Identify the blood parasite species.
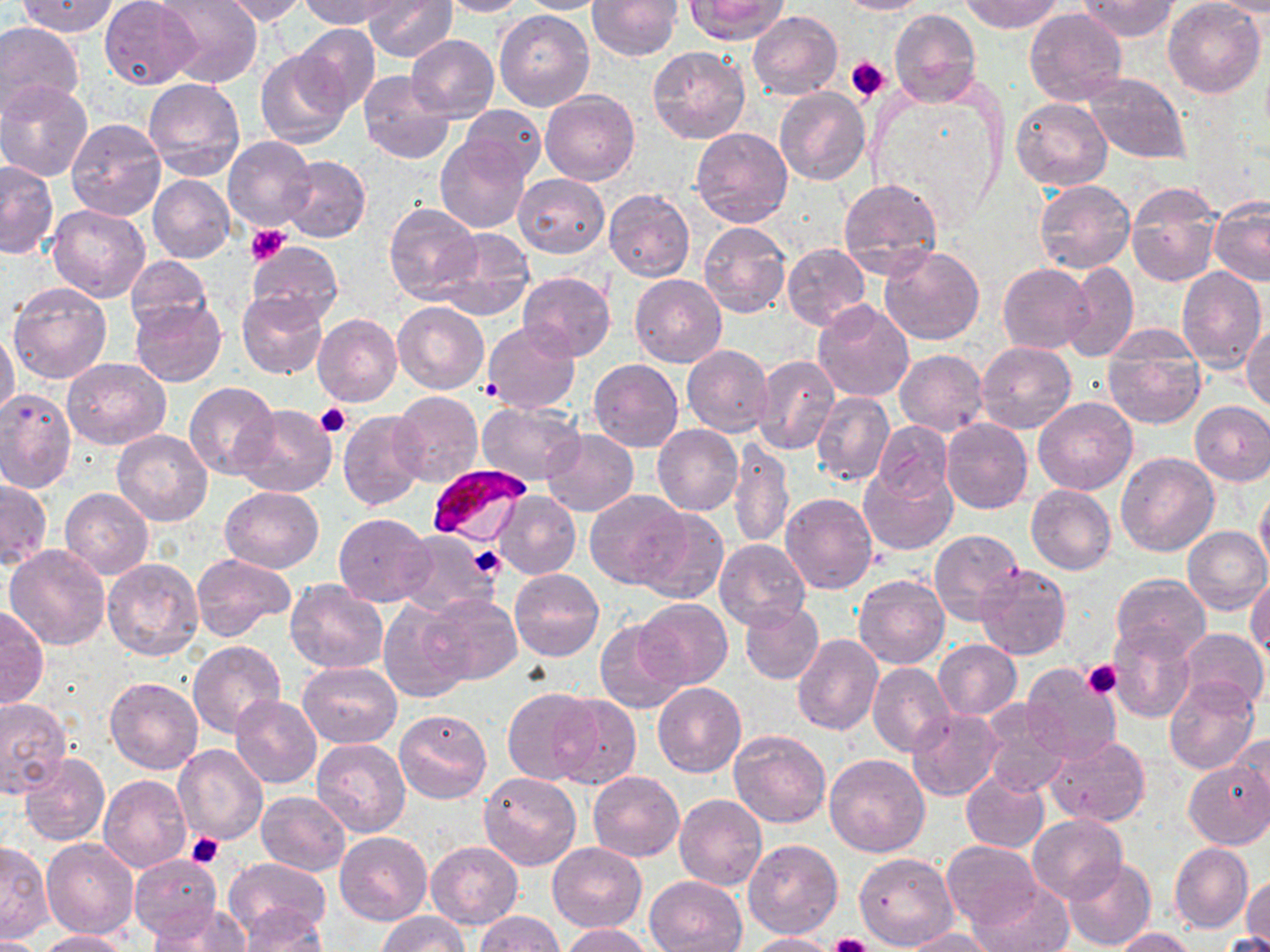

Plasmodium falciparum.

Approximate bounding boxes as named x1/y1/x2/y2 corners in pixels. Platelet locations: (x1=846, y1=55, x2=892, y2=101), (x1=244, y1=225, x2=291, y2=266), (x1=480, y1=379, x2=503, y2=403), (x1=316, y1=403, x2=352, y2=438), (x1=468, y1=546, x2=505, y2=577), (x1=1082, y1=659, x2=1121, y2=700), (x1=186, y1=833, x2=223, y2=869), (x1=826, y1=933, x2=875, y2=952). Uninfected red blood cell locations: (x1=17, y1=0, x2=119, y2=36), (x1=99, y1=0, x2=201, y2=88), (x1=154, y1=0, x2=262, y2=88), (x1=210, y1=0, x2=313, y2=25), (x1=301, y1=0, x2=396, y2=28), (x1=361, y1=0, x2=457, y2=62), (x1=436, y1=0, x2=527, y2=16), (x1=515, y1=0, x2=613, y2=13), (x1=586, y1=0, x2=681, y2=60), (x1=685, y1=0, x2=787, y2=44), (x1=835, y1=0, x2=931, y2=14), (x1=961, y1=0, x2=1062, y2=33), (x1=1076, y1=0, x2=1181, y2=40), (x1=1164, y1=1, x2=1265, y2=99), (x1=1207, y1=1, x2=1270, y2=15), (x1=495, y1=8, x2=594, y2=111), (x1=1024, y1=8, x2=1127, y2=108), (x1=890, y1=9, x2=982, y2=109), (x1=748, y1=10, x2=843, y2=100), (x1=0, y1=23, x2=83, y2=119), (x1=294, y1=25, x2=381, y2=112), (x1=407, y1=35, x2=498, y2=121), (x1=647, y1=45, x2=751, y2=144), (x1=255, y1=48, x2=351, y2=149), (x1=357, y1=70, x2=455, y2=164), (x1=1085, y1=73, x2=1190, y2=165), (x1=144, y1=79, x2=245, y2=182), (x1=0, y1=82, x2=92, y2=182), (x1=774, y1=87, x2=869, y2=186), (x1=540, y1=90, x2=640, y2=185), (x1=1012, y1=98, x2=1112, y2=191), (x1=460, y1=104, x2=546, y2=182), (x1=66, y1=118, x2=167, y2=222), (x1=690, y1=128, x2=792, y2=227), (x1=224, y1=136, x2=318, y2=232), (x1=435, y1=137, x2=530, y2=233), (x1=280, y1=155, x2=370, y2=242), (x1=0, y1=161, x2=58, y2=258), (x1=515, y1=173, x2=608, y2=257), (x1=148, y1=175, x2=235, y2=263), (x1=838, y1=177, x2=944, y2=279), (x1=1035, y1=181, x2=1135, y2=273), (x1=1125, y1=181, x2=1222, y2=287), (x1=605, y1=190, x2=695, y2=281), (x1=1209, y1=199, x2=1270, y2=287), (x1=384, y1=203, x2=482, y2=303), (x1=48, y1=205, x2=150, y2=302), (x1=698, y1=221, x2=791, y2=319), (x1=434, y1=227, x2=534, y2=321), (x1=246, y1=242, x2=343, y2=327), (x1=782, y1=243, x2=869, y2=330), (x1=880, y1=246, x2=983, y2=345), (x1=125, y1=257, x2=213, y2=335), (x1=1062, y1=261, x2=1139, y2=362), (x1=998, y1=263, x2=1094, y2=354), (x1=1177, y1=265, x2=1267, y2=370), (x1=517, y1=272, x2=616, y2=361), (x1=629, y1=274, x2=726, y2=367), (x1=8, y1=280, x2=112, y2=384), (x1=238, y1=291, x2=327, y2=378), (x1=131, y1=300, x2=227, y2=388), (x1=392, y1=302, x2=488, y2=394), (x1=813, y1=302, x2=915, y2=404), (x1=312, y1=313, x2=403, y2=407), (x1=483, y1=321, x2=581, y2=414), (x1=1243, y1=325, x2=1270, y2=413), (x1=0, y1=329, x2=20, y2=425), (x1=1101, y1=337, x2=1207, y2=430), (x1=977, y1=341, x2=1076, y2=432), (x1=681, y1=345, x2=773, y2=437), (x1=895, y1=349, x2=988, y2=437), (x1=753, y1=355, x2=840, y2=455), (x1=61, y1=358, x2=171, y2=450), (x1=589, y1=359, x2=683, y2=452), (x1=185, y1=383, x2=279, y2=480), (x1=0, y1=388, x2=76, y2=493), (x1=390, y1=390, x2=485, y2=486), (x1=811, y1=392, x2=894, y2=486), (x1=1034, y1=398, x2=1137, y2=496), (x1=476, y1=400, x2=584, y2=485), (x1=1189, y1=401, x2=1270, y2=486), (x1=233, y1=403, x2=336, y2=499), (x1=338, y1=410, x2=426, y2=510), (x1=942, y1=419, x2=1032, y2=513), (x1=872, y1=422, x2=953, y2=503), (x1=652, y1=424, x2=742, y2=515), (x1=542, y1=429, x2=638, y2=516), (x1=113, y1=430, x2=212, y2=527), (x1=728, y1=439, x2=795, y2=549), (x1=1116, y1=451, x2=1219, y2=557), (x1=860, y1=463, x2=956, y2=554), (x1=1, y1=480, x2=51, y2=569), (x1=1255, y1=483, x2=1270, y2=575), (x1=1025, y1=485, x2=1115, y2=574), (x1=220, y1=486, x2=325, y2=573), (x1=60, y1=487, x2=153, y2=579), (x1=583, y1=488, x2=684, y2=588), (x1=492, y1=490, x2=580, y2=580), (x1=781, y1=494, x2=878, y2=595), (x1=633, y1=507, x2=729, y2=604), (x1=333, y1=512, x2=434, y2=606), (x1=1183, y1=527, x2=1270, y2=614), (x1=397, y1=529, x2=503, y2=619), (x1=928, y1=529, x2=1022, y2=625), (x1=714, y1=539, x2=809, y2=628), (x1=6, y1=543, x2=110, y2=651), (x1=192, y1=553, x2=295, y2=638), (x1=102, y1=558, x2=204, y2=661), (x1=975, y1=563, x2=1071, y2=660), (x1=509, y1=568, x2=604, y2=662), (x1=1247, y1=571, x2=1270, y2=661), (x1=1112, y1=574, x2=1210, y2=659), (x1=854, y1=575, x2=950, y2=669), (x1=285, y1=579, x2=390, y2=674), (x1=424, y1=595, x2=521, y2=684), (x1=635, y1=598, x2=732, y2=690), (x1=379, y1=600, x2=473, y2=702), (x1=740, y1=602, x2=823, y2=684), (x1=0, y1=606, x2=48, y2=710), (x1=596, y1=620, x2=689, y2=716), (x1=1108, y1=625, x2=1195, y2=724), (x1=1179, y1=627, x2=1269, y2=709), (x1=792, y1=635, x2=883, y2=736), (x1=934, y1=640, x2=1022, y2=721), (x1=187, y1=641, x2=286, y2=739), (x1=298, y1=662, x2=402, y2=747), (x1=868, y1=662, x2=954, y2=757), (x1=1020, y1=662, x2=1121, y2=763), (x1=105, y1=676, x2=202, y2=775), (x1=1165, y1=678, x2=1259, y2=774), (x1=652, y1=682, x2=746, y2=776), (x1=501, y1=687, x2=601, y2=785), (x1=549, y1=692, x2=641, y2=790), (x1=230, y1=695, x2=322, y2=788), (x1=0, y1=699, x2=72, y2=799), (x1=982, y1=703, x2=1070, y2=797), (x1=393, y1=709, x2=491, y2=804), (x1=908, y1=709, x2=1002, y2=802), (x1=728, y1=729, x2=831, y2=828), (x1=1232, y1=732, x2=1270, y2=814), (x1=1046, y1=734, x2=1150, y2=827), (x1=311, y1=738, x2=410, y2=838), (x1=173, y1=744, x2=269, y2=846), (x1=19, y1=754, x2=109, y2=846), (x1=824, y1=754, x2=932, y2=857), (x1=1183, y1=761, x2=1270, y2=849), (x1=479, y1=771, x2=582, y2=870), (x1=588, y1=771, x2=684, y2=861), (x1=961, y1=771, x2=1049, y2=854), (x1=98, y1=775, x2=191, y2=873), (x1=257, y1=791, x2=352, y2=875), (x1=674, y1=794, x2=767, y2=892), (x1=1027, y1=816, x2=1126, y2=902), (x1=335, y1=832, x2=433, y2=925), (x1=41, y1=839, x2=139, y2=940), (x1=744, y1=839, x2=842, y2=937), (x1=942, y1=840, x2=1041, y2=930), (x1=425, y1=841, x2=523, y2=929), (x1=1, y1=842, x2=53, y2=944), (x1=547, y1=842, x2=647, y2=931), (x1=1169, y1=842, x2=1253, y2=932), (x1=854, y1=852, x2=958, y2=950), (x1=129, y1=854, x2=221, y2=942), (x1=225, y1=858, x2=331, y2=942), (x1=1063, y1=859, x2=1156, y2=951), (x1=1242, y1=873, x2=1270, y2=951), (x1=644, y1=875, x2=746, y2=952), (x1=967, y1=880, x2=1074, y2=952), (x1=148, y1=903, x2=251, y2=952), (x1=235, y1=903, x2=327, y2=951), (x1=377, y1=911, x2=470, y2=951), (x1=474, y1=911, x2=564, y2=951), (x1=558, y1=923, x2=654, y2=952), (x1=1112, y1=927, x2=1197, y2=951), (x1=894, y1=928, x2=1001, y2=951), (x1=35, y1=930, x2=130, y2=952), (x1=1221, y1=930, x2=1269, y2=952), (x1=741, y1=931, x2=839, y2=951), (x1=0, y1=935, x2=46, y2=952). Plasmodium falciparum-infected red blood cell locations: (x1=426, y1=461, x2=533, y2=545). 1000x magnification. Thin blood film. Single field of view. Image is 1270×952 pixels. Optical microscopy. May-Grünwald-Giemsa-stained preparation.